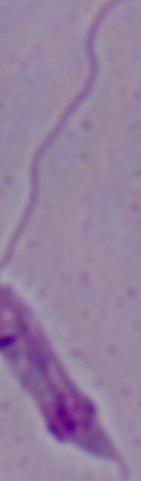
A Leishmania parasite is shown. 1000x magnification. Photomicrograph.